Outline each Plasmodium vivax-infected red blood cell.
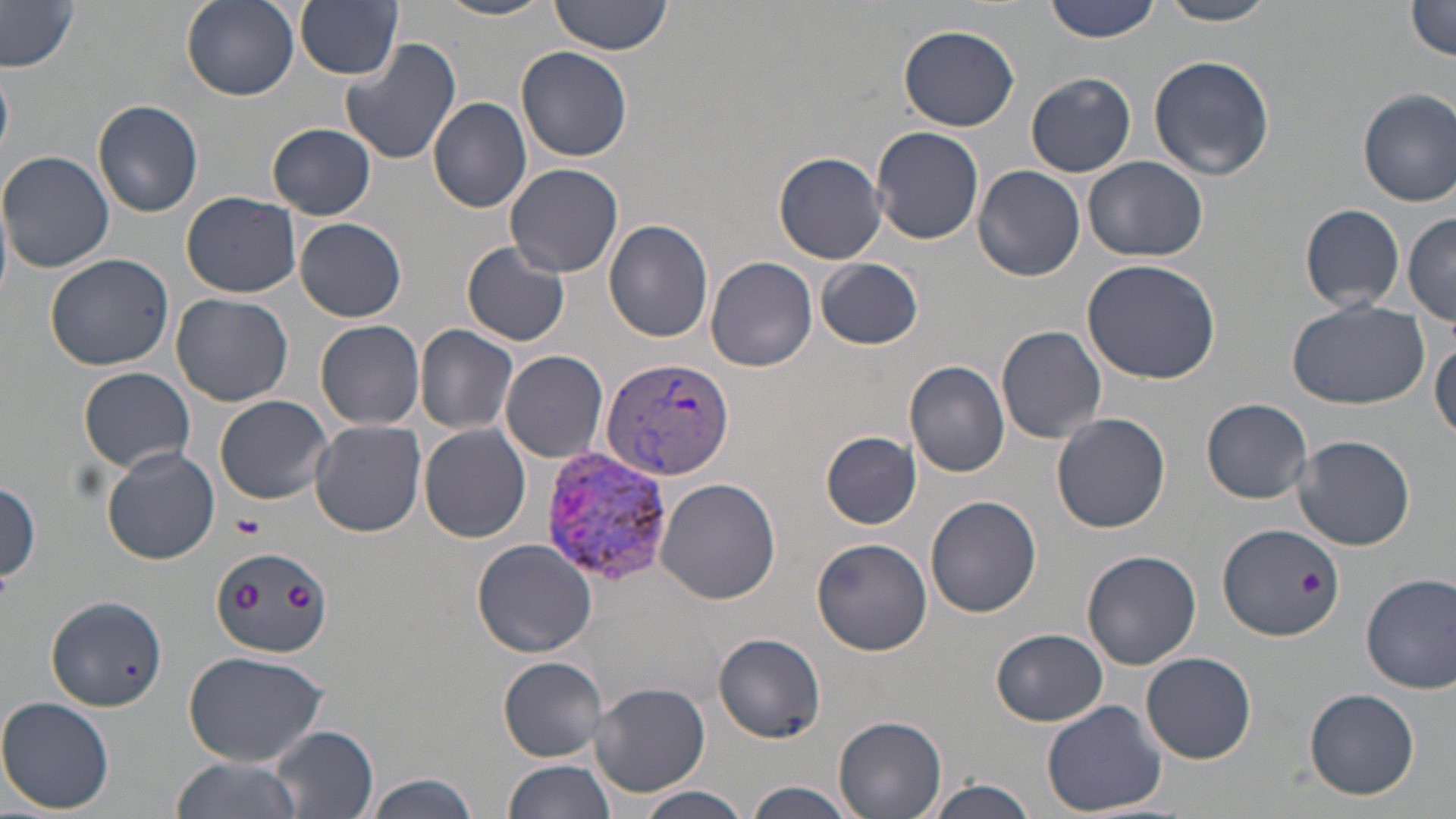

Approximate bounding boxes as named x1/y1/x2/y2 corners in pixels.
Plasmodium vivax-infected red blood cells: (x1=599, y1=356, x2=736, y2=482), (x1=541, y1=448, x2=677, y2=587).

Uninfected red blood cell locations: (x1=182, y1=0, x2=299, y2=101), (x1=297, y1=0, x2=403, y2=79), (x1=549, y1=0, x2=675, y2=56), (x1=1045, y1=0, x2=1165, y2=44), (x1=1158, y1=0, x2=1281, y2=25), (x1=436, y1=1, x2=556, y2=22), (x1=1406, y1=2, x2=1456, y2=61), (x1=0, y1=4, x2=81, y2=72), (x1=898, y1=23, x2=1021, y2=131), (x1=340, y1=38, x2=461, y2=167), (x1=516, y1=46, x2=633, y2=163), (x1=1147, y1=54, x2=1274, y2=180), (x1=0, y1=65, x2=13, y2=157), (x1=1026, y1=72, x2=1135, y2=176), (x1=1358, y1=89, x2=1456, y2=205), (x1=428, y1=97, x2=531, y2=214), (x1=92, y1=99, x2=204, y2=217), (x1=268, y1=123, x2=375, y2=219), (x1=871, y1=126, x2=985, y2=245), (x1=0, y1=150, x2=114, y2=274), (x1=774, y1=151, x2=887, y2=263), (x1=1085, y1=156, x2=1207, y2=262), (x1=505, y1=164, x2=624, y2=279), (x1=972, y1=165, x2=1085, y2=281), (x1=182, y1=190, x2=301, y2=297), (x1=1300, y1=203, x2=1405, y2=312), (x1=1404, y1=213, x2=1456, y2=324), (x1=296, y1=218, x2=406, y2=322), (x1=604, y1=219, x2=715, y2=342), (x1=462, y1=243, x2=571, y2=347), (x1=45, y1=252, x2=175, y2=372), (x1=706, y1=256, x2=818, y2=371), (x1=817, y1=259, x2=924, y2=349), (x1=1081, y1=259, x2=1222, y2=386), (x1=172, y1=294, x2=292, y2=406), (x1=1285, y1=298, x2=1427, y2=409), (x1=317, y1=320, x2=425, y2=430), (x1=415, y1=324, x2=518, y2=434), (x1=996, y1=325, x2=1106, y2=443), (x1=1430, y1=338, x2=1455, y2=445), (x1=501, y1=348, x2=609, y2=462), (x1=904, y1=361, x2=1011, y2=476), (x1=79, y1=366, x2=196, y2=473), (x1=215, y1=395, x2=334, y2=504), (x1=1202, y1=398, x2=1313, y2=503), (x1=1052, y1=413, x2=1172, y2=534), (x1=310, y1=420, x2=426, y2=536), (x1=419, y1=426, x2=532, y2=543), (x1=822, y1=431, x2=922, y2=529), (x1=1291, y1=435, x2=1417, y2=551), (x1=102, y1=446, x2=220, y2=564), (x1=657, y1=479, x2=782, y2=606), (x1=0, y1=480, x2=42, y2=585), (x1=925, y1=496, x2=1042, y2=617), (x1=1218, y1=523, x2=1347, y2=642), (x1=812, y1=537, x2=932, y2=656), (x1=472, y1=539, x2=598, y2=658), (x1=211, y1=547, x2=332, y2=658), (x1=1081, y1=549, x2=1201, y2=668), (x1=1361, y1=573, x2=1456, y2=694), (x1=45, y1=595, x2=167, y2=714), (x1=992, y1=628, x2=1107, y2=724), (x1=712, y1=631, x2=826, y2=743), (x1=182, y1=650, x2=331, y2=768), (x1=1141, y1=651, x2=1257, y2=764), (x1=498, y1=657, x2=610, y2=761), (x1=588, y1=680, x2=711, y2=798), (x1=1303, y1=687, x2=1421, y2=800), (x1=0, y1=696, x2=116, y2=814), (x1=1041, y1=700, x2=1168, y2=818), (x1=832, y1=716, x2=946, y2=819), (x1=271, y1=725, x2=377, y2=818), (x1=170, y1=758, x2=302, y2=819), (x1=502, y1=758, x2=617, y2=819), (x1=361, y1=773, x2=482, y2=819), (x1=919, y1=780, x2=1040, y2=819), (x1=745, y1=781, x2=859, y2=819), (x1=631, y1=787, x2=757, y2=819). Platelet locations: (x1=234, y1=514, x2=265, y2=540). Slide-level diagnosis: Plasmodium vivax. Thin blood smear. Optical microscopy. 1000x magnification. One field of a larger specimen. May-Grünwald-Giemsa-stained preparation. Image is 1456×819 pixels.